Outline each blood parasite and name the species.
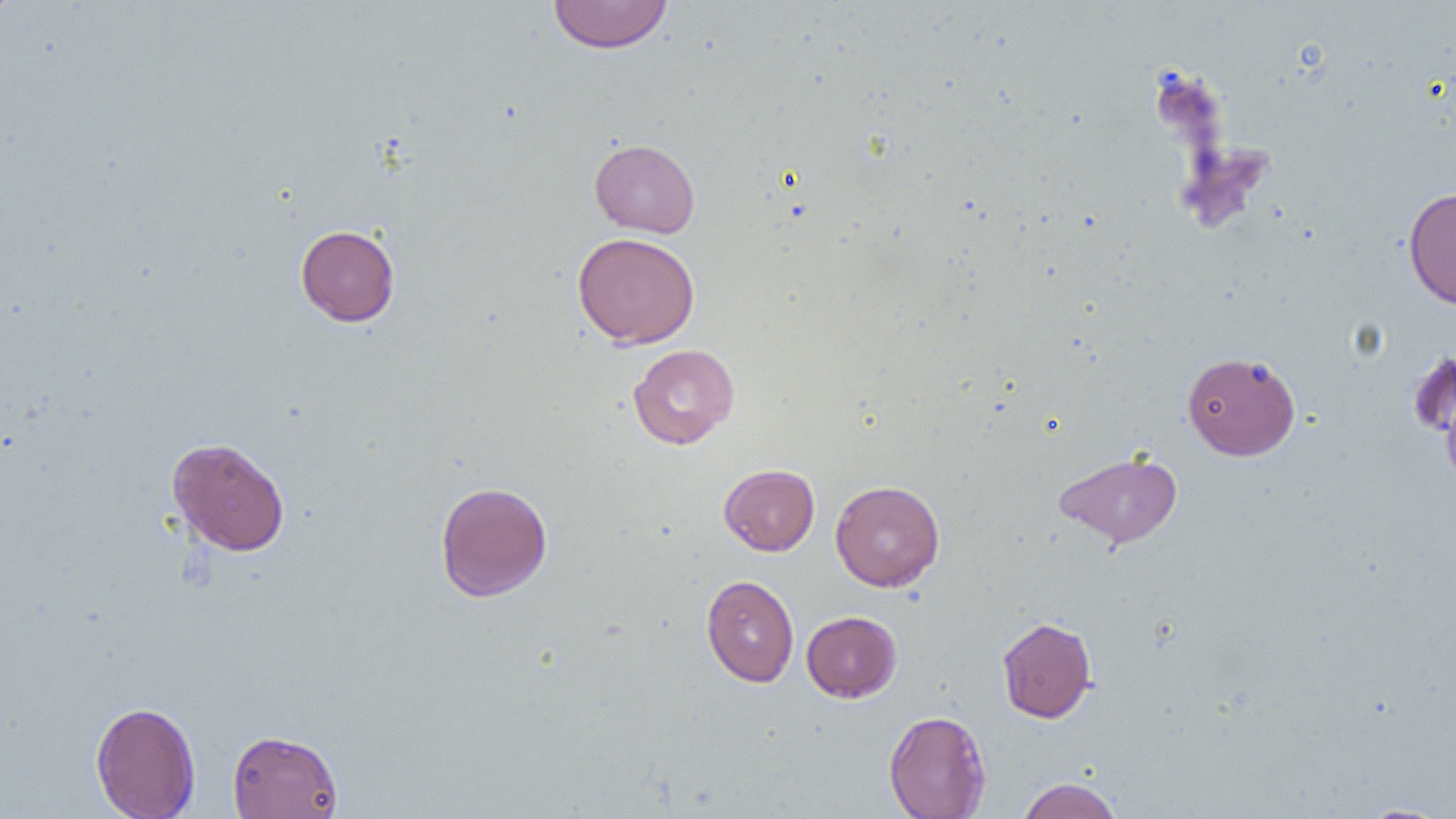
No blood parasites observed.

Summary:
  - Coordinate format: approximate bounding boxes as (x1, y1, x2, y2) in pixels
  - Uninfected red blood cell locations: (548, 0, 673, 54), (589, 139, 700, 238), (1403, 186, 1456, 310), (295, 224, 400, 327), (572, 231, 700, 348), (628, 343, 740, 449), (1407, 348, 1456, 444), (1182, 351, 1300, 460), (1441, 378, 1456, 496), (167, 437, 290, 556), (1054, 450, 1182, 548), (718, 464, 820, 556), (830, 480, 945, 591), (434, 481, 552, 602), (701, 574, 799, 687), (801, 611, 901, 702), (996, 616, 1097, 723), (90, 701, 201, 819), (884, 710, 991, 819), (227, 729, 344, 818), (1017, 777, 1123, 819), (1354, 803, 1452, 818)
  - Slide-level diagnosis: no evidence of blood parasites
  - Image size: 1456×819 pixels
  - Preparation: thin blood film
  - Modality: light microscopy
  - Field of view: single
  - Magnification: 1000x